Describe the morphology of the red blood cells.
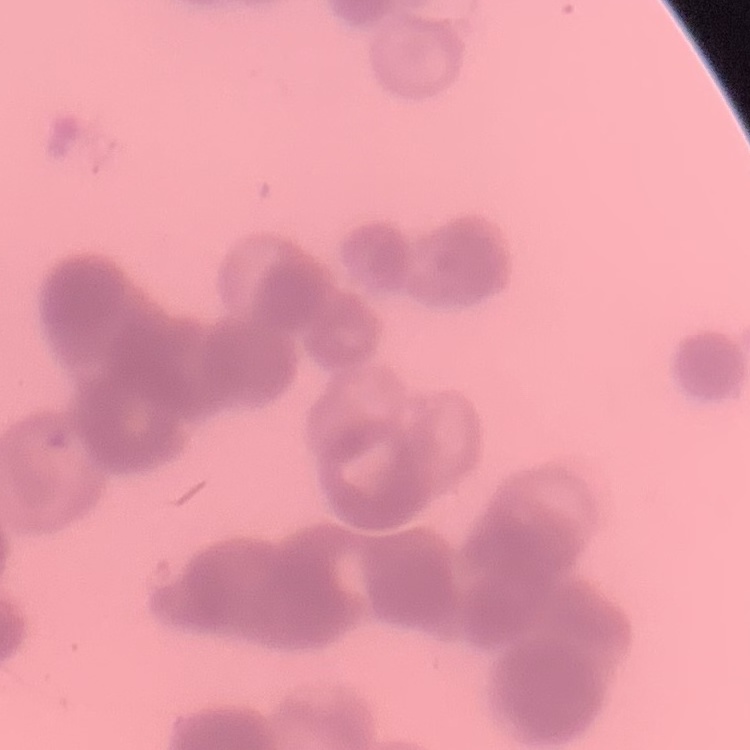

They show rouleaux formation.

Summary:
  - Preparation: thin blood film
  - Image type: one tile cut from a larger photomicrograph
  - Stain: Field's or Giemsa